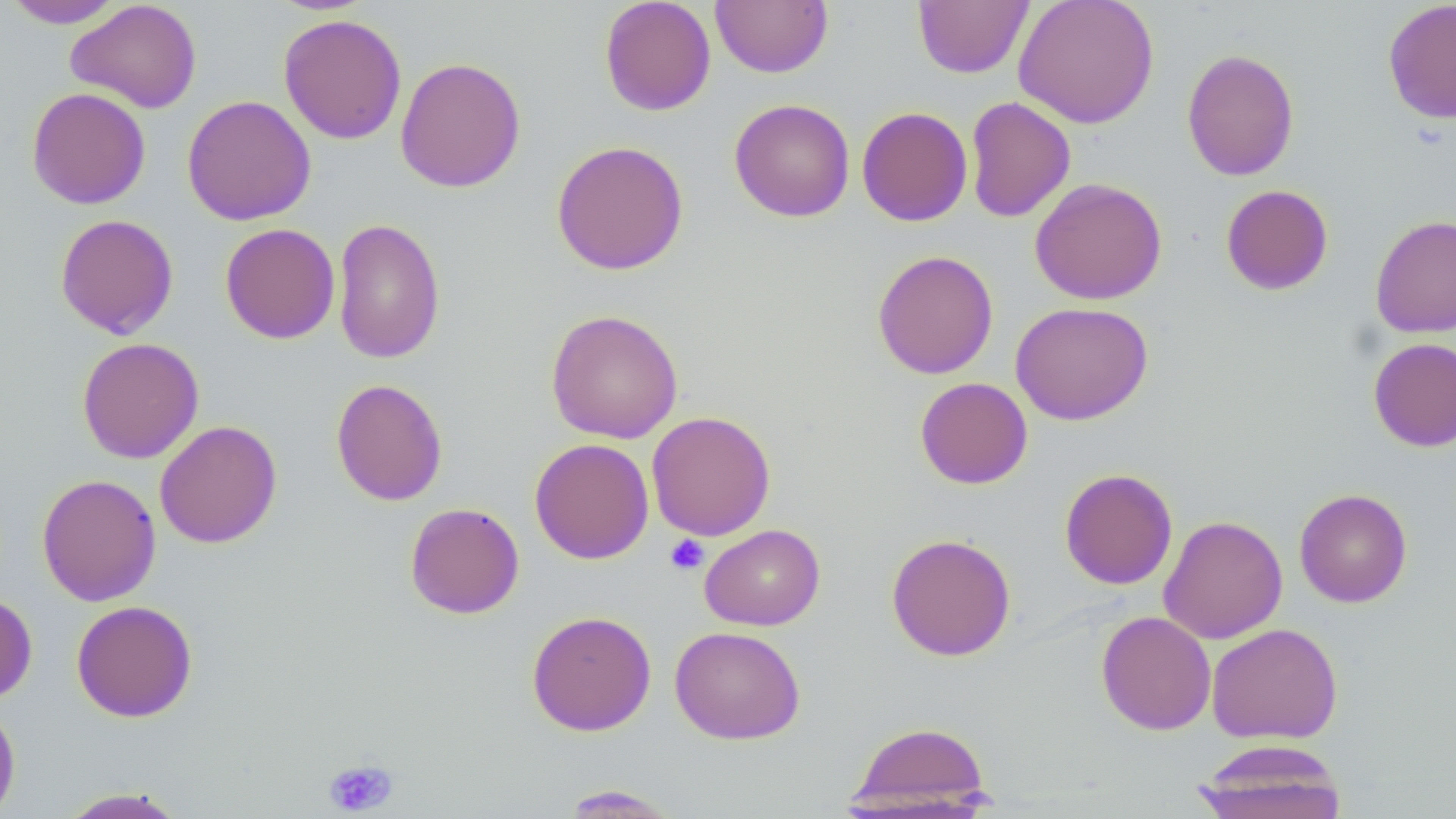

Summary:
  - Coordinate format: approximate bounding boxes as named x1/y1/x2/y2 corners in pixels
  - Platelet locations: (x1=665, y1=534, x2=709, y2=575), (x1=323, y1=757, x2=399, y2=816)
  - Uninfected red blood cell locations: (x1=65, y1=0, x2=202, y2=113), (x1=599, y1=0, x2=717, y2=116), (x1=710, y1=0, x2=833, y2=78), (x1=1013, y1=0, x2=1160, y2=128), (x1=1382, y1=0, x2=1456, y2=124), (x1=2, y1=1, x2=126, y2=28), (x1=913, y1=1, x2=1033, y2=79), (x1=278, y1=13, x2=407, y2=145), (x1=1181, y1=48, x2=1300, y2=181), (x1=395, y1=56, x2=526, y2=193), (x1=26, y1=87, x2=151, y2=209), (x1=182, y1=95, x2=316, y2=226), (x1=964, y1=96, x2=1076, y2=223), (x1=729, y1=98, x2=855, y2=223), (x1=856, y1=106, x2=973, y2=226), (x1=551, y1=139, x2=689, y2=276), (x1=1029, y1=177, x2=1167, y2=305), (x1=1220, y1=184, x2=1334, y2=295), (x1=54, y1=213, x2=179, y2=339), (x1=1370, y1=214, x2=1456, y2=338), (x1=332, y1=217, x2=445, y2=364), (x1=219, y1=223, x2=340, y2=344), (x1=872, y1=249, x2=999, y2=379), (x1=1010, y1=301, x2=1154, y2=425), (x1=545, y1=309, x2=684, y2=443), (x1=76, y1=337, x2=204, y2=463), (x1=1368, y1=337, x2=1456, y2=452), (x1=915, y1=377, x2=1033, y2=490), (x1=330, y1=378, x2=448, y2=506), (x1=646, y1=411, x2=776, y2=541), (x1=154, y1=420, x2=282, y2=548), (x1=529, y1=438, x2=654, y2=564), (x1=1059, y1=468, x2=1178, y2=590), (x1=36, y1=473, x2=161, y2=606), (x1=1294, y1=487, x2=1413, y2=608), (x1=404, y1=502, x2=525, y2=619), (x1=1159, y1=515, x2=1288, y2=644), (x1=699, y1=524, x2=825, y2=631), (x1=886, y1=533, x2=1017, y2=661), (x1=0, y1=591, x2=37, y2=705), (x1=71, y1=600, x2=198, y2=722), (x1=526, y1=610, x2=657, y2=736), (x1=1096, y1=611, x2=1217, y2=735), (x1=1207, y1=623, x2=1343, y2=744), (x1=669, y1=626, x2=806, y2=744), (x1=0, y1=699, x2=21, y2=819), (x1=845, y1=720, x2=995, y2=814), (x1=1191, y1=740, x2=1349, y2=819), (x1=558, y1=785, x2=681, y2=817), (x1=57, y1=787, x2=189, y2=818)
  - Slide-level diagnosis: negative for blood parasites
  - Modality: light microscopy
  - Preparation: thin blood film
  - Image size: 1456×819 pixels
  - Stain: May-Grünwald-Giemsa
  - Magnification: 1000x
  - Field of view: one of a larger specimen